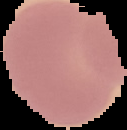
Summary:
  - Preparation: thin blood smear
  - Image size: 127×130 pixels
  - Image type: segmented cell region on a black background
  - Result: negative for malaria parasites